Locate every blood parasite and identify its species.
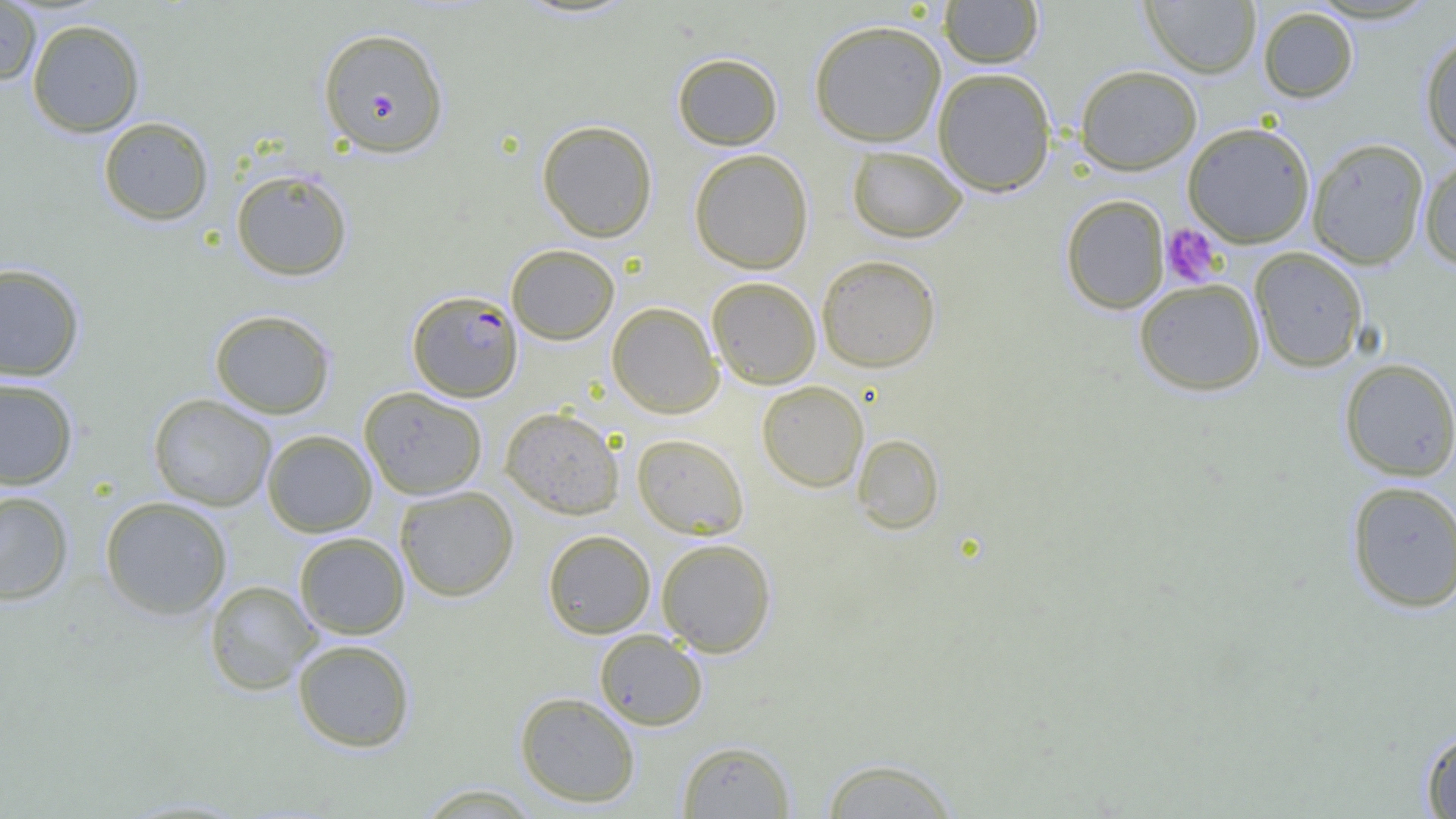
Approximate bounding boxes as (x1, y1, x2, y2) in pixels.
Plasmodium falciparum-infected red blood cells: (318, 27, 449, 158), (407, 290, 523, 402).
No Plasmodium ovale, Plasmodium malariae, Plasmodium vivax, Babesia divergens, or Trypanosoma brucei observed.

Platelet locations: (1160, 223, 1223, 287). Uninfected red blood cell locations: (939, 0, 1043, 68), (1141, 0, 1262, 78), (0, 1, 42, 86), (1258, 6, 1358, 103), (27, 18, 145, 137), (809, 19, 947, 146), (1419, 31, 1456, 157), (672, 52, 783, 150), (1074, 64, 1202, 175), (932, 67, 1057, 197), (98, 117, 214, 225), (537, 119, 658, 242), (1182, 121, 1316, 247), (1306, 137, 1430, 270), (846, 146, 968, 243), (689, 148, 814, 274), (1419, 155, 1456, 270), (230, 169, 353, 281), (1060, 194, 1170, 314), (506, 244, 620, 344), (1249, 247, 1368, 372), (816, 254, 941, 372), (0, 263, 85, 381), (706, 276, 822, 389), (1133, 278, 1266, 396), (607, 302, 724, 418), (209, 309, 335, 418), (1338, 358, 1456, 482), (0, 377, 79, 489), (757, 380, 869, 492), (359, 386, 487, 500), (149, 393, 277, 511), (500, 406, 624, 519), (263, 429, 377, 537), (631, 433, 749, 539), (853, 433, 944, 534), (1345, 480, 1456, 613), (394, 485, 519, 602), (0, 491, 74, 605), (99, 496, 233, 620), (542, 529, 656, 638), (294, 532, 410, 639), (656, 538, 776, 656), (205, 580, 320, 695), (594, 629, 708, 731), (292, 639, 416, 753), (514, 692, 641, 808), (1421, 728, 1456, 818), (677, 740, 794, 818), (819, 756, 961, 818), (414, 783, 545, 818). Slide-level diagnosis: Plasmodium falciparum. Thin blood film. Image is 1456×819 pixels. One field of a larger specimen. Captured at 1000x magnification. Light microscopy.